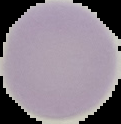
Summary:
  - Preparation: thin blood film
  - Image size: 121×124 pixels
  - Malaria status: uninfected
  - Image type: segmented cell region on a black background